Describe the morphology of the erythrocytes.
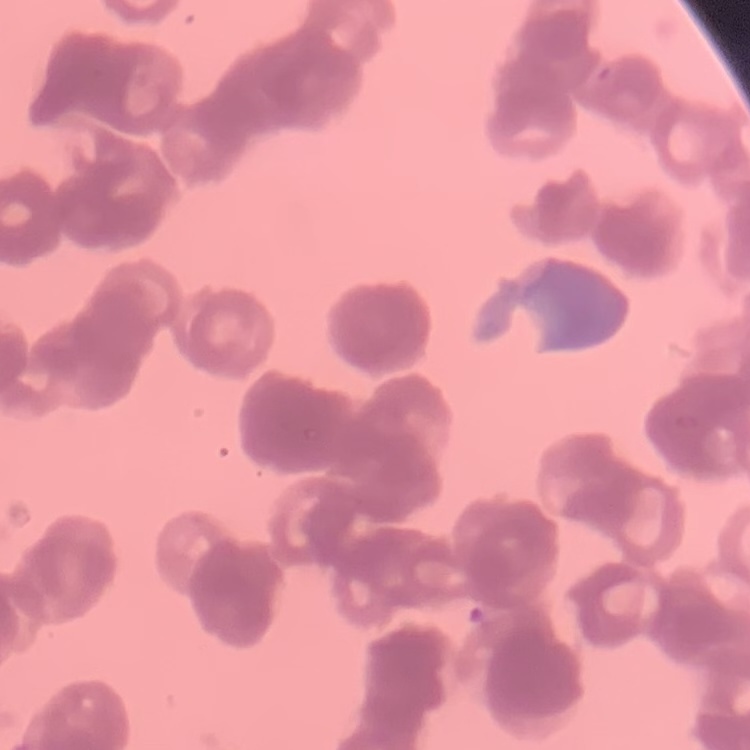
They show rouleaux formation.

preparation = thin blood smear
stain = Field's or Giemsa
image type = one tile cut from a larger photomicrograph